Locate every Plasmodium falciparum-infected red blood cell.
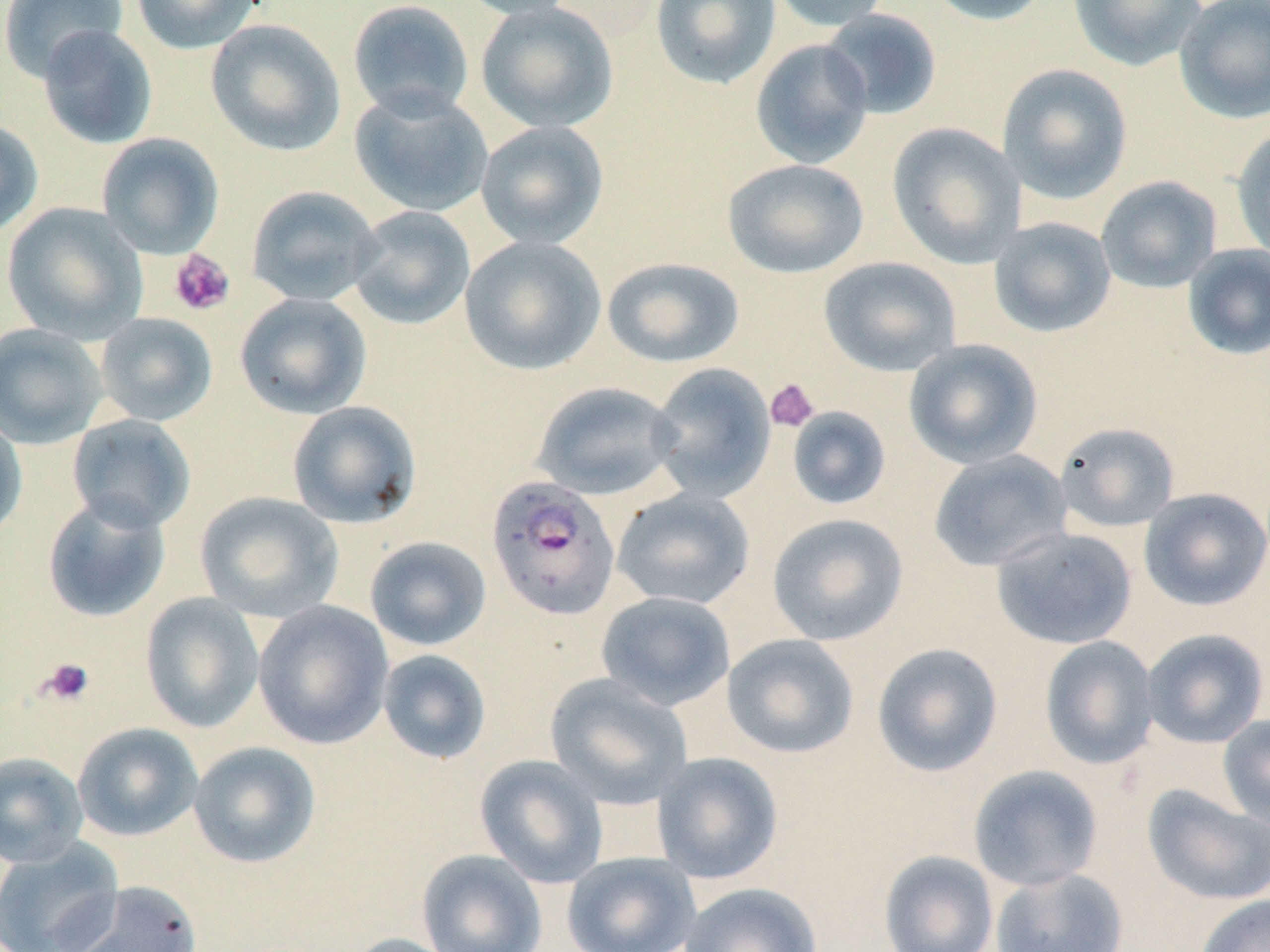

Approximate bounding boxes as (x1,y1)-(x2,y2) corner pairs in pixels.
Plasmodium falciparum-infected red blood cells: (485,476)-(621,621).

Uninfected red blood cell locations: (130,0)-(263,55), (455,0)-(580,21), (650,0)-(781,90), (764,0)-(895,32), (922,0)-(1052,26), (1068,0)-(1206,71), (1173,0)-(1270,124), (0,1)-(128,83), (347,1)-(474,120), (475,2)-(618,134), (819,8)-(942,120), (206,18)-(346,157), (37,25)-(158,149), (749,38)-(875,169), (996,63)-(1133,204), (350,88)-(493,217), (0,117)-(44,238), (475,121)-(609,249), (887,122)-(1027,268), (1231,125)-(1270,261), (96,132)-(225,259), (722,158)-(870,279), (1096,175)-(1222,293), (246,185)-(383,307), (2,202)-(147,342), (348,206)-(476,330), (988,217)-(1116,337), (459,235)-(605,375), (1182,243)-(1270,361), (602,256)-(745,368), (819,256)-(961,376), (235,292)-(372,419), (94,312)-(218,427), (0,323)-(108,448), (903,338)-(1043,469), (647,362)-(776,503), (531,381)-(683,500), (287,400)-(422,528), (786,406)-(892,510), (0,412)-(28,543), (66,414)-(196,533), (1054,422)-(1180,532), (928,449)-(1073,571), (612,488)-(756,610), (1139,488)-(1270,611), (195,491)-(344,623), (42,494)-(171,623), (767,513)-(909,646), (990,526)-(1138,649), (364,536)-(492,651), (595,591)-(735,711), (140,593)-(264,733), (253,600)-(394,749), (1141,628)-(1269,749), (722,633)-(859,759), (1039,635)-(1159,770), (871,642)-(1003,777), (377,649)-(491,764), (545,673)-(694,809), (1218,713)-(1270,831), (72,722)-(203,841), (188,741)-(321,868), (0,751)-(89,868), (651,751)-(784,884), (474,754)-(609,888), (968,764)-(1103,891), (1142,784)-(1270,906), (0,838)-(124,952), (417,849)-(547,952), (878,849)-(999,952), (561,851)-(701,952), (990,867)-(1129,952), (58,880)-(203,952), (679,882)-(823,952), (1194,893)-(1270,952), (340,933)-(463,952). Platelet locations: (168,250)-(235,317), (764,378)-(820,433), (39,657)-(95,707). Slide-level diagnosis: Plasmodium falciparum. Image is 1270×952 pixels. Thin blood film. May-Grünwald-Giemsa-stained preparation. Captured at 1000x magnification. One field of a larger specimen. Optical microscopy.